State which cell type is depicted.
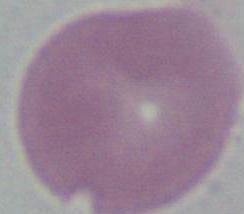
This is an erythrocyte.

magnification = 1000x
modality = micrograph